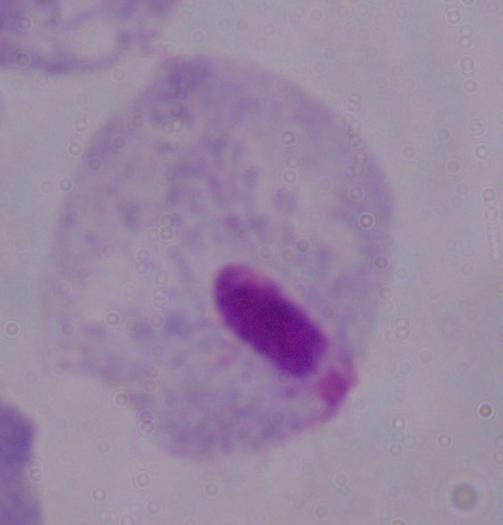

identification = trichomonad
modality = micrograph
magnification = 1000x